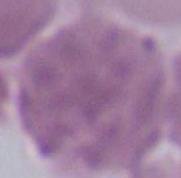
magnification = 1000x
identification = red blood cell
modality = micrograph